Locate every malaria parasite and every leukocyte.
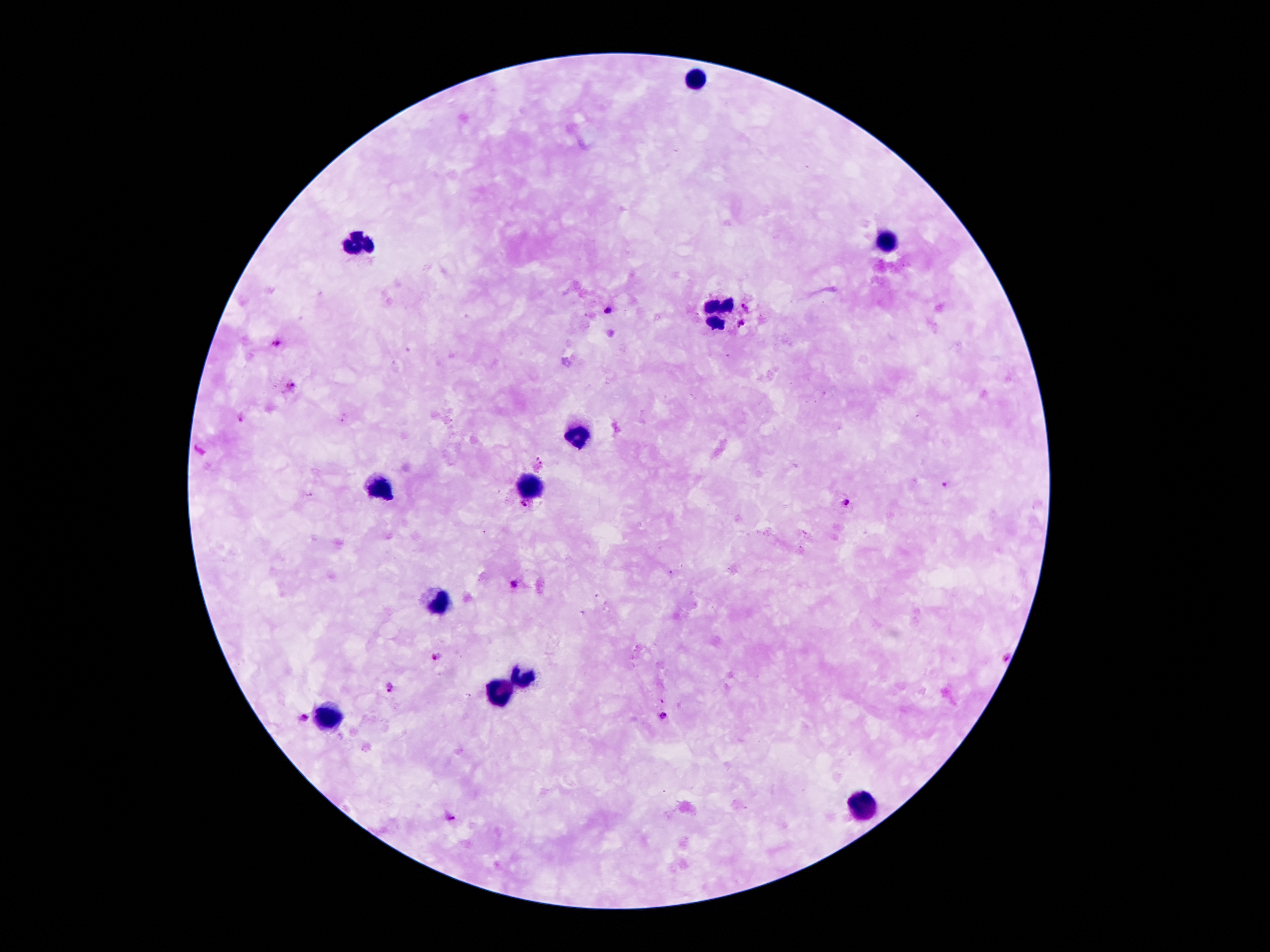
Approximate centers as [x, y] in pixels.
Malaria parasites: [748, 307], [607, 310], [742, 324], [275, 343], [293, 385], [242, 417], [945, 484], [849, 501], [525, 506], [513, 583], [437, 655], [1005, 659], [391, 688], [664, 716], [305, 717], [450, 816].
Leukocytes: [695, 80], [887, 243], [355, 245], [721, 311], [579, 434], [377, 484], [531, 486], [439, 602], [525, 678], [499, 691], [327, 714], [863, 807].

Summary:
  - Image size: 1270×952 pixels
  - Capture: smartphone through the microscope eyepiece
  - Stain: Giemsa
  - Magnification: 100x
  - Patient malaria status: positive for Plasmodium falciparum
  - Preparation: thick peripheral-blood smear
  - Field of view: single